Outline each blood parasite and name the species.
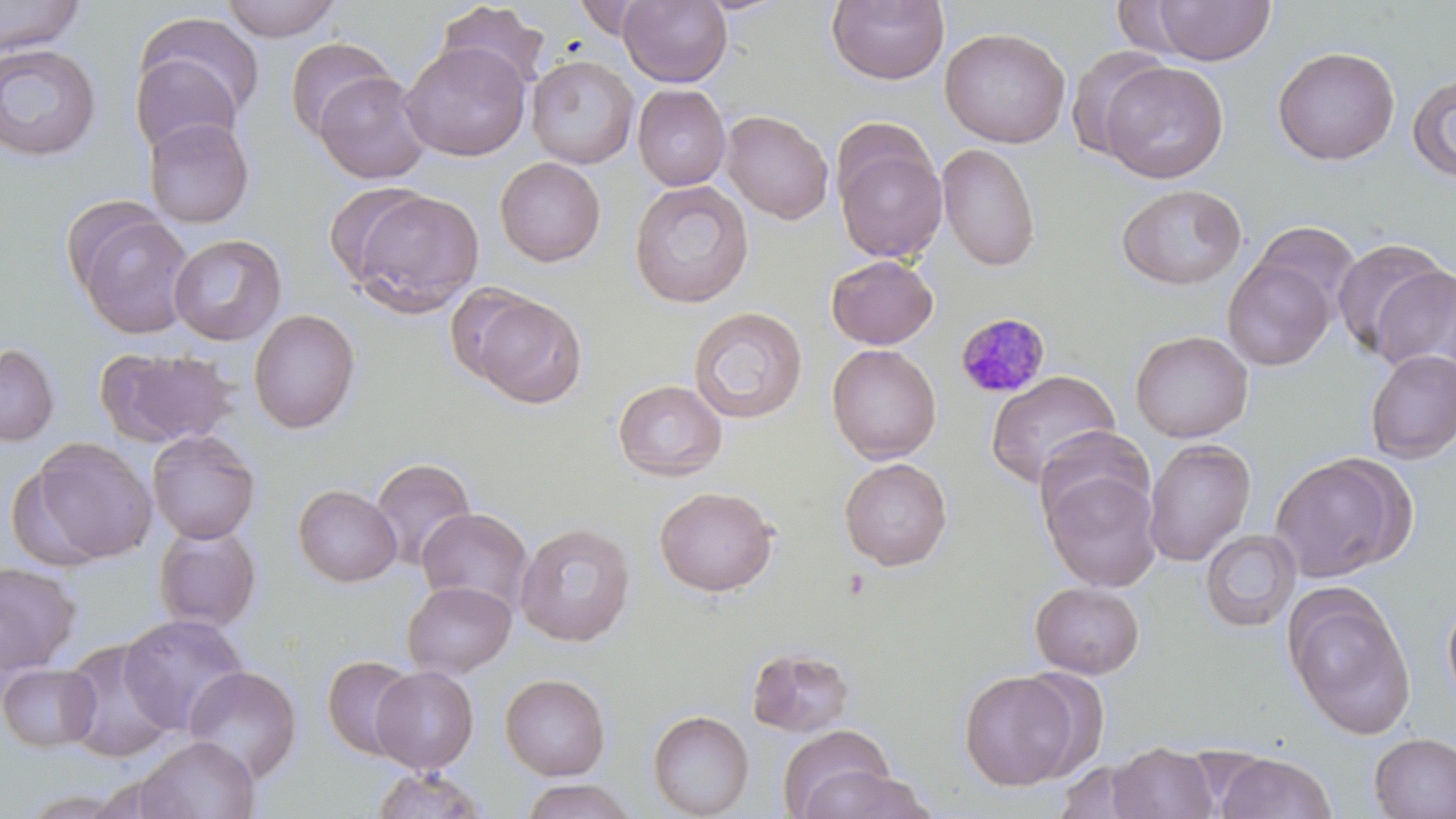
Approximate bounding boxes as [x1, y1, x2, y2] in pixels.
Plasmodium malariae-infected red blood cells: [957, 312, 1054, 397].
No Plasmodium falciparum, Plasmodium ovale, Plasmodium vivax, Babesia divergens, or Trypanosoma brucei observed.

Summary:
  - Uninfected red blood cell locations: [0, 0, 88, 56], [219, 0, 344, 42], [571, 0, 655, 39], [619, 0, 733, 88], [826, 0, 949, 86], [1146, 1, 1276, 65], [434, 2, 551, 93], [132, 12, 265, 135], [939, 27, 1071, 148], [284, 37, 396, 140], [400, 41, 531, 161], [0, 43, 102, 161], [1065, 45, 1172, 160], [1272, 45, 1400, 166], [527, 55, 639, 169], [137, 56, 246, 182], [1099, 60, 1229, 183], [313, 70, 430, 184], [1407, 73, 1456, 181], [633, 84, 731, 191], [720, 110, 834, 225], [143, 117, 255, 228], [833, 129, 948, 265], [937, 143, 1040, 271], [495, 156, 605, 267], [628, 180, 754, 309], [324, 181, 431, 286], [1116, 184, 1247, 291], [345, 188, 484, 317], [69, 205, 195, 339], [1253, 221, 1362, 319], [168, 233, 287, 346], [1331, 237, 1452, 359], [826, 254, 939, 350], [1222, 254, 1337, 370], [1372, 266, 1456, 377], [467, 292, 588, 409], [689, 306, 807, 424], [247, 308, 361, 434], [1130, 330, 1253, 443], [0, 343, 59, 446], [826, 344, 942, 465], [96, 346, 237, 448], [1365, 350, 1456, 464], [986, 371, 1120, 489], [613, 379, 727, 482], [1032, 426, 1155, 529], [147, 429, 261, 545], [31, 438, 157, 564], [1142, 438, 1257, 567], [1269, 452, 1412, 583], [370, 457, 476, 570], [839, 457, 953, 571], [1042, 467, 1163, 591], [293, 484, 402, 587], [654, 486, 779, 597], [416, 507, 534, 615], [514, 522, 636, 647], [154, 526, 262, 632], [1200, 529, 1301, 632], [0, 561, 83, 674], [402, 581, 517, 679], [1030, 581, 1145, 679], [1284, 587, 1417, 739], [1442, 594, 1456, 708], [118, 614, 250, 736], [59, 638, 178, 763], [746, 646, 855, 738], [322, 655, 422, 761], [0, 663, 102, 752], [182, 665, 302, 785], [370, 666, 479, 774], [1015, 667, 1112, 778], [958, 670, 1082, 791], [500, 673, 611, 780], [648, 710, 754, 818], [777, 723, 897, 819], [1368, 732, 1456, 819], [135, 735, 260, 819], [1108, 742, 1219, 819], [1215, 752, 1337, 818], [1053, 759, 1159, 819], [797, 765, 939, 818], [370, 767, 488, 818], [518, 779, 640, 819], [20, 788, 141, 818]
  - Slide-level diagnosis: Plasmodium malariae
  - Field of view: single
  - Modality: light microscopy
  - Image size: 1456×819 pixels
  - Magnification: 1000x
  - Stain: May-Grünwald-Giemsa
  - Preparation: thin blood smear